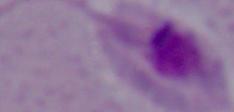

magnification = 1000x
modality = micrograph
identification = Leishmania